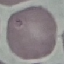
Summary:
  - Malaria status: uninfected
  - Capture: smartphone through the microscope eyepiece
  - Image type: cell patch, automatically extracted from a larger field of view and resized to 64 × 64 pixels
  - Stain: Giemsa
  - Preparation: thin blood film